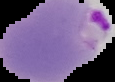
image_size: 115×82 pixels
malaria_status: parasitized
preparation: thin blood film
image_type: segmented cell region on a black background